Outline each Plasmodium ovale-infected red blood cell.
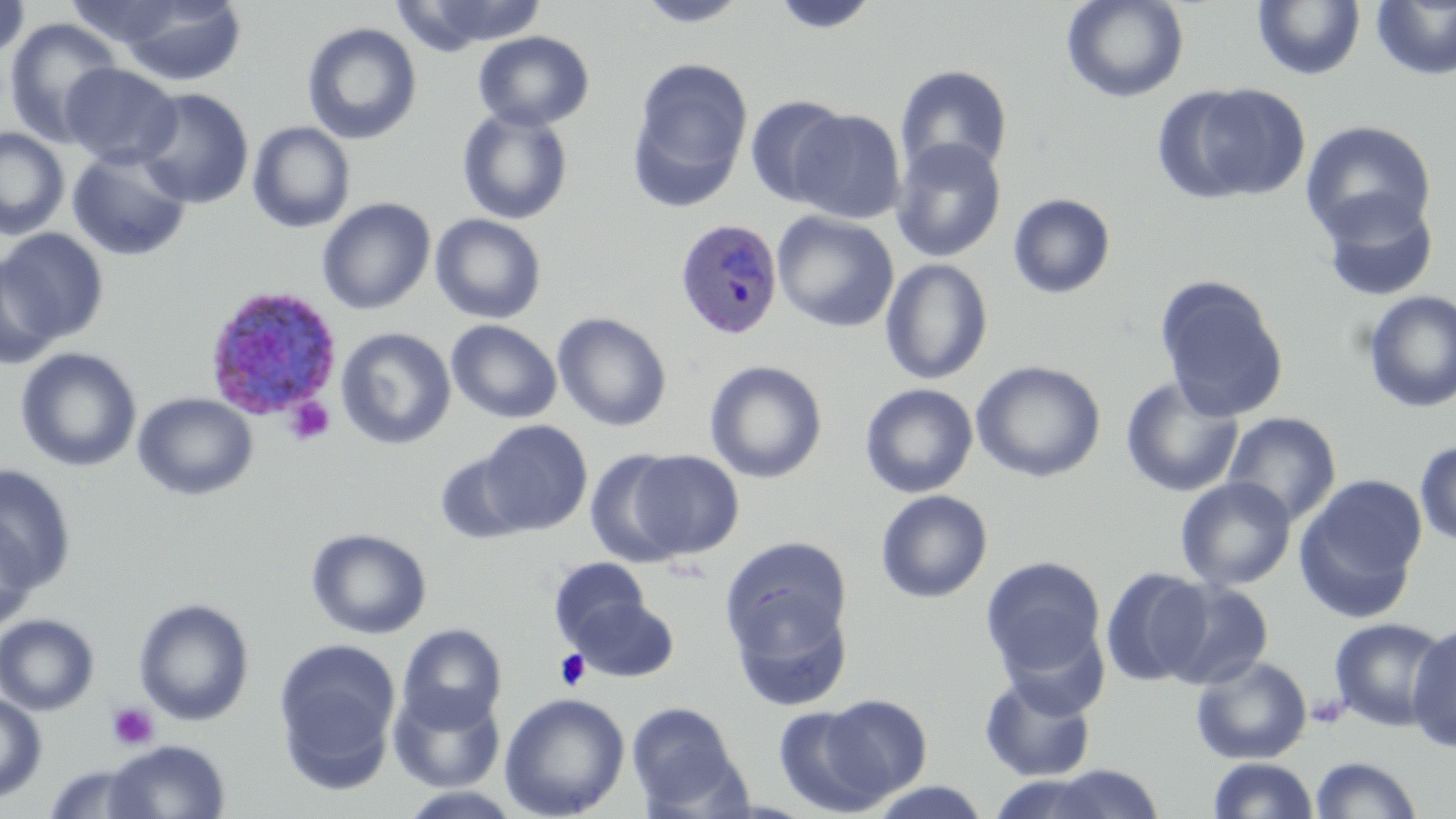

Approximate bounding boxes as (x1, y1, x2, y2) in pixels.
Plasmodium ovale-infected red blood cells: (674, 218, 783, 341), (202, 285, 346, 417).

Uninfected red blood cell locations: (0, 0, 31, 64), (634, 0, 752, 27), (771, 0, 881, 35), (1061, 0, 1189, 103), (111, 1, 248, 86), (394, 1, 549, 52), (1252, 1, 1366, 80), (1371, 1, 1456, 81), (3, 18, 124, 147), (301, 22, 422, 145), (473, 31, 595, 132), (629, 57, 753, 207), (60, 63, 182, 169), (894, 64, 1013, 179), (1158, 84, 1312, 206), (135, 87, 254, 208), (744, 94, 852, 208), (457, 108, 573, 226), (790, 109, 905, 224), (1300, 120, 1437, 245), (247, 122, 356, 233), (0, 127, 70, 239), (890, 137, 1007, 263), (67, 149, 192, 262), (1315, 190, 1440, 303), (1007, 193, 1117, 299), (316, 197, 435, 314), (772, 211, 899, 333), (430, 214, 547, 324), (1, 229, 108, 348), (0, 256, 62, 370), (880, 258, 993, 385), (1154, 275, 1290, 422), (1362, 290, 1456, 414), (553, 312, 671, 432), (446, 319, 562, 423), (336, 327, 456, 450), (15, 347, 141, 473), (705, 360, 828, 484), (971, 360, 1106, 483), (1119, 376, 1244, 499), (860, 383, 978, 498), (132, 392, 258, 501), (1222, 411, 1342, 526), (478, 420, 593, 535), (1414, 440, 1456, 547), (586, 450, 691, 567), (628, 450, 743, 559), (434, 451, 532, 545), (0, 463, 78, 597), (1295, 475, 1428, 619), (1176, 477, 1296, 591), (875, 490, 993, 603), (0, 516, 38, 634), (306, 527, 432, 639), (719, 534, 854, 677), (981, 556, 1107, 680), (549, 557, 650, 647), (1100, 567, 1213, 686), (1159, 579, 1274, 690), (133, 597, 254, 726), (571, 597, 678, 683), (0, 613, 100, 715), (1328, 617, 1450, 731), (999, 621, 1108, 720), (397, 623, 507, 731), (1406, 623, 1456, 753), (273, 638, 400, 785), (1190, 655, 1313, 765), (980, 673, 1096, 782), (389, 686, 505, 793), (0, 693, 47, 803), (499, 693, 630, 818), (817, 693, 932, 802), (625, 701, 746, 815), (773, 706, 894, 817), (104, 739, 230, 819), (1309, 755, 1423, 818), (1207, 757, 1319, 818), (42, 762, 157, 817), (1036, 764, 1168, 819), (865, 780, 994, 819). Platelet locations: (284, 395, 337, 445), (554, 649, 591, 692), (107, 701, 159, 751). Slide-level diagnosis: Plasmodium ovale. May-Grünwald-Giemsa-stained preparation. Optical microscopy. Thin blood film. Image is 1456×819 pixels. 1000x magnification. Single field of view.